Classify this cell by malaria status.
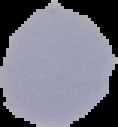
Uninfected.

image type = segmented cell region with the area outside set to black
preparation = thin blood smear
image size = 118×127 pixels